Give the extent of all Plasmodium malariae-infected red blood cells.
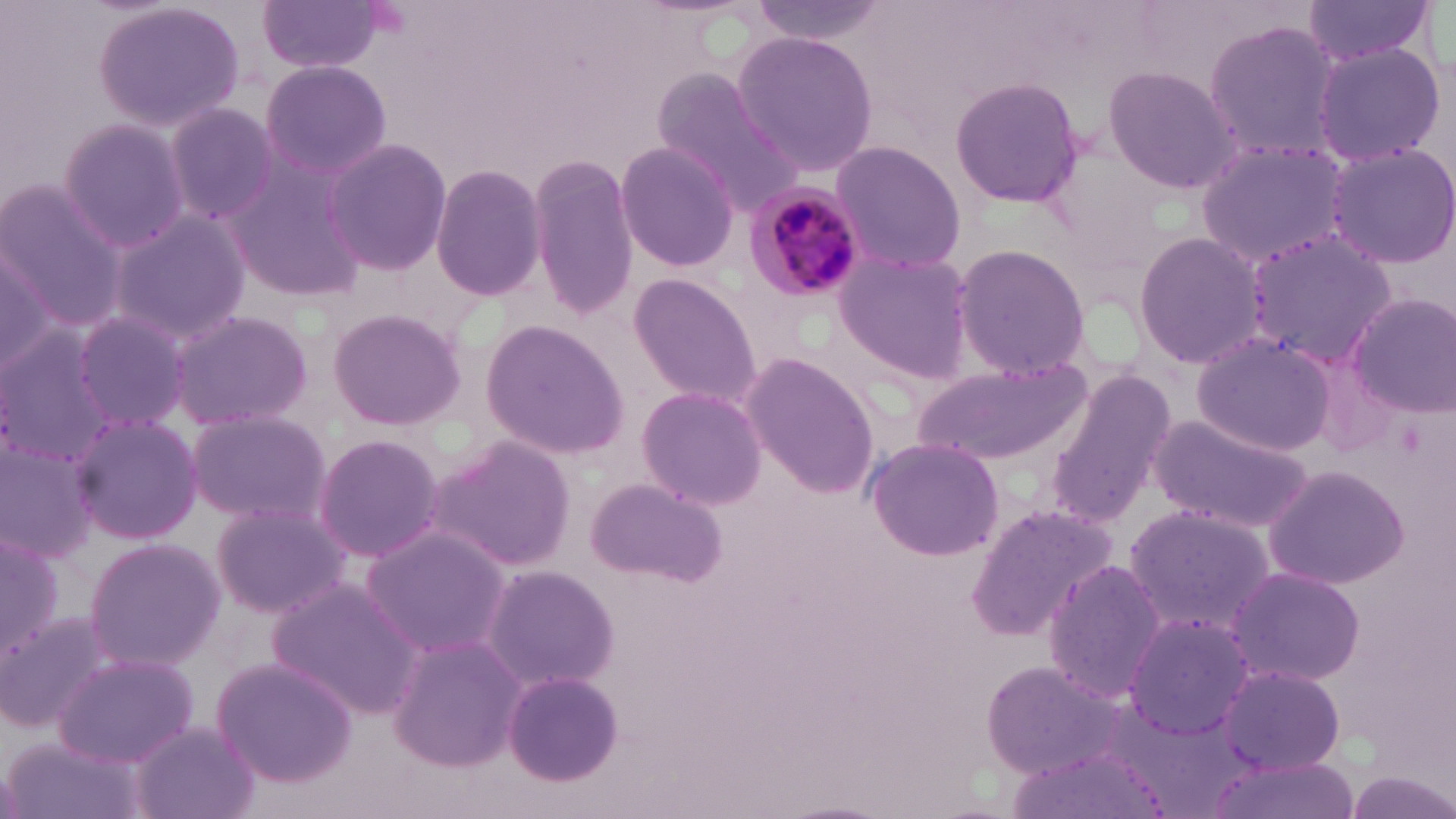
Approximate bounding boxes as [x1, y1, x2, y2] in pixels.
Plasmodium malariae-infected red blood cells: [741, 187, 868, 305].

Uninfected red blood cell locations: [256, 0, 389, 74], [746, 0, 893, 42], [1299, 0, 1437, 66], [93, 1, 246, 133], [1201, 18, 1348, 163], [731, 30, 879, 177], [1311, 42, 1445, 166], [260, 60, 391, 180], [1101, 63, 1243, 195], [651, 71, 804, 215], [950, 75, 1085, 210], [163, 101, 283, 227], [56, 117, 193, 253], [322, 137, 451, 276], [828, 138, 966, 274], [1196, 138, 1356, 270], [614, 139, 740, 272], [1323, 141, 1456, 269], [222, 151, 371, 303], [528, 153, 642, 319], [429, 162, 547, 300], [0, 180, 124, 329], [108, 209, 253, 345], [1242, 228, 1397, 363], [1133, 232, 1264, 372], [0, 240, 67, 383], [951, 242, 1091, 379], [833, 247, 974, 382], [626, 271, 763, 407], [1344, 291, 1456, 419], [324, 307, 469, 431], [171, 309, 313, 430], [68, 310, 193, 431], [480, 318, 630, 459], [0, 326, 120, 463], [1191, 332, 1334, 455], [738, 349, 880, 497], [913, 357, 1090, 467], [1045, 366, 1174, 527], [634, 384, 768, 509], [184, 408, 332, 527], [66, 412, 204, 544], [1147, 412, 1318, 536], [0, 431, 99, 563], [311, 432, 445, 564], [429, 435, 578, 571], [864, 436, 1003, 561], [1262, 464, 1408, 590], [586, 476, 728, 588], [209, 501, 350, 619], [966, 502, 1116, 643], [1124, 504, 1276, 639], [357, 525, 513, 657], [0, 532, 62, 665], [83, 536, 225, 671], [1041, 557, 1167, 700], [482, 565, 620, 688], [1225, 566, 1364, 685], [266, 579, 420, 719], [0, 609, 119, 736], [1121, 612, 1255, 743], [387, 632, 523, 771], [55, 653, 197, 768], [209, 655, 359, 788], [980, 659, 1134, 779], [1216, 662, 1346, 775], [501, 669, 623, 785], [127, 720, 261, 819], [6, 735, 147, 819], [1008, 750, 1162, 818], [1206, 757, 1361, 819], [1341, 769, 1456, 816]. Slide-level diagnosis: Plasmodium malariae. Image is 1456×819 pixels. Light microscopy. Thin blood smear. Captured at 1000x magnification. One field of a larger specimen. May-Grünwald-Giemsa stain.